Report the malaria status of this cell.
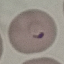

It is parasitized.

Summary:
  - Image type: automatically extracted cell patch, resized to 64 × 64 pixels
  - Capture: smartphone camera at the microscope eyepiece
  - Preparation: thin smear
  - Stain: Giemsa